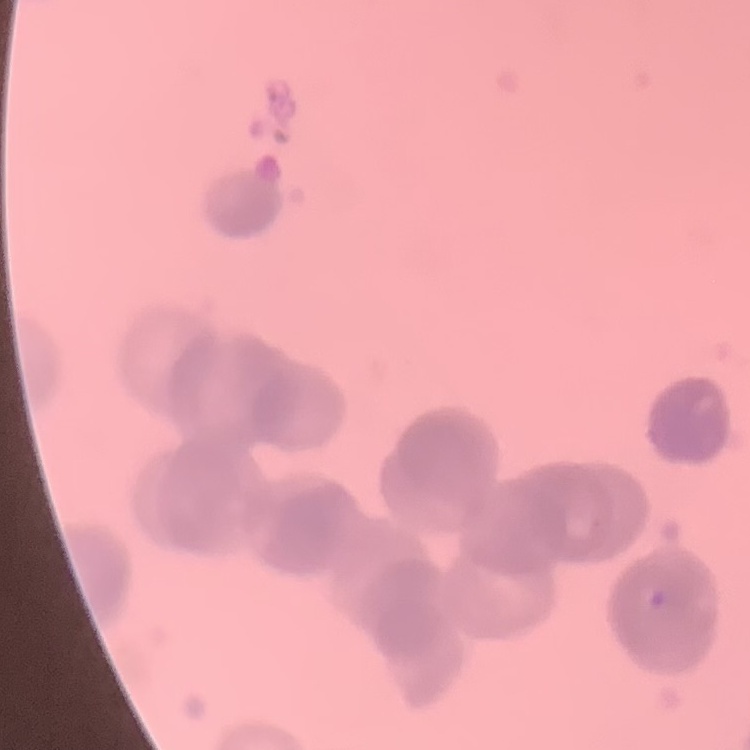 The erythrocytes exhibit rouleaux formation. Thin blood smear. Stained with either Field's or Giemsa. Square crop of a larger photomicrograph.